State which cell type is depicted.
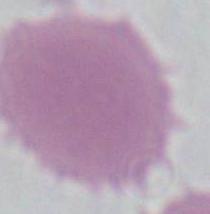

This is an erythrocyte.

Summary:
  - Modality: micrograph
  - Magnification: 1000x